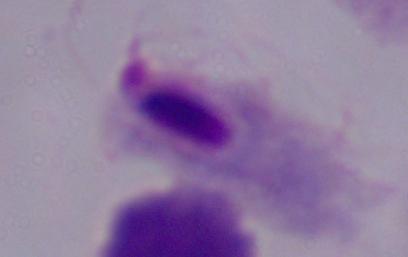
magnification: 1000x
modality: photomicrograph
identification: trichomonad